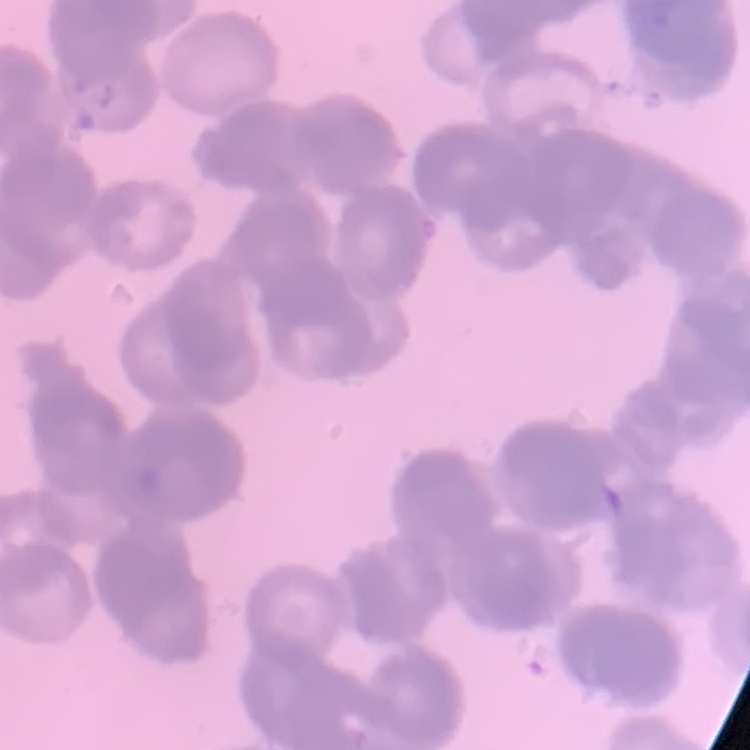

Summary:
  - Red blood cell morphology: rouleaux formation
  - Preparation: thin blood smear
  - Stain: Field's or Giemsa
  - Image type: one tile cut from a larger photomicrograph